Give the position of every Plasmodium parasite visible.
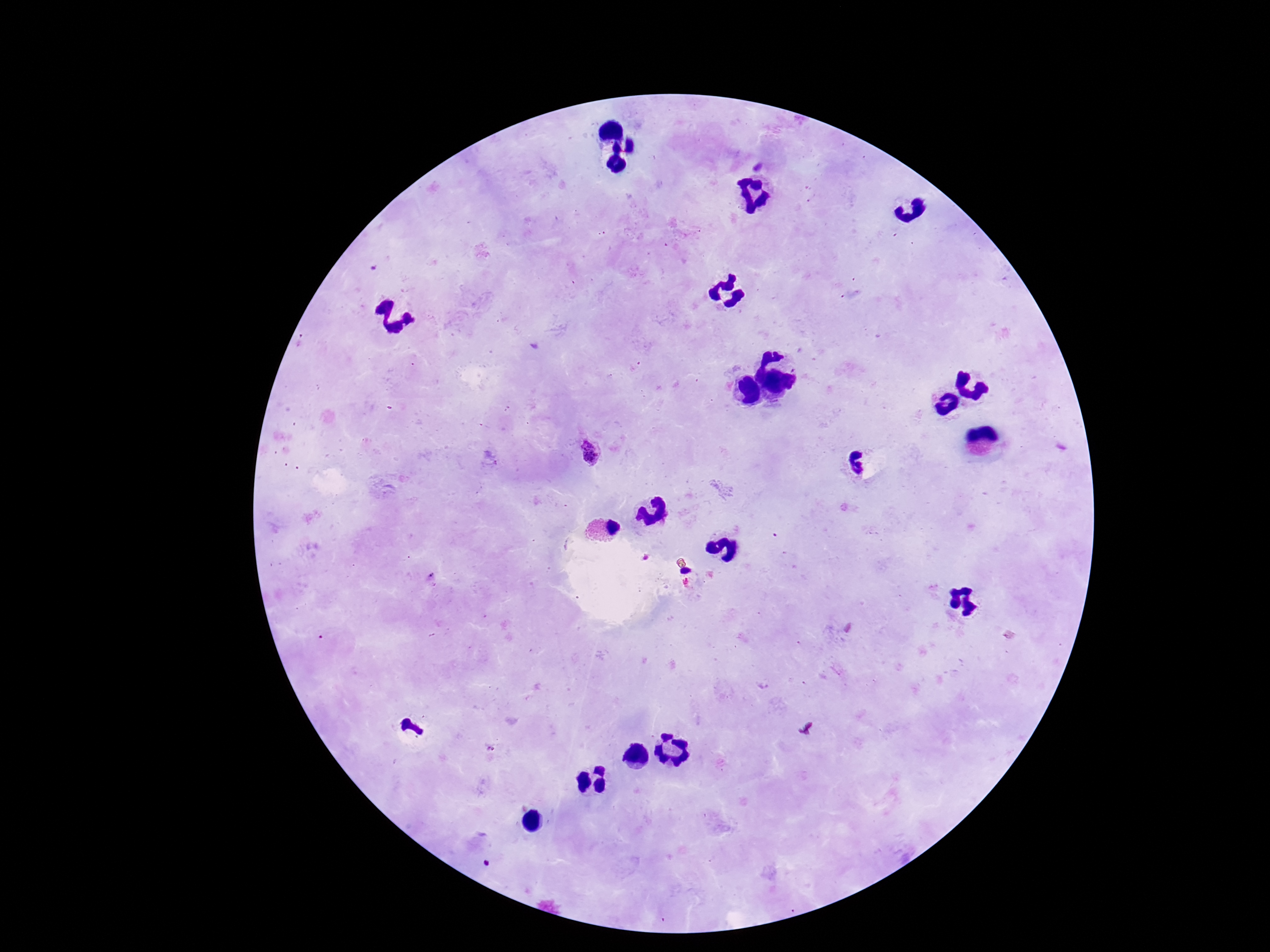
Approximate object centers, in pixels from the top-left corner.
Plasmodium parasites: (x=591, y=453).

preparation = thick blood smear
field of view = one from this slide
patient malaria status = positive
stain = Giemsa
magnification = 100x
image size = 1270×952 pixels
capture = smartphone camera through the microscope eyepiece